Name the parasite shown.
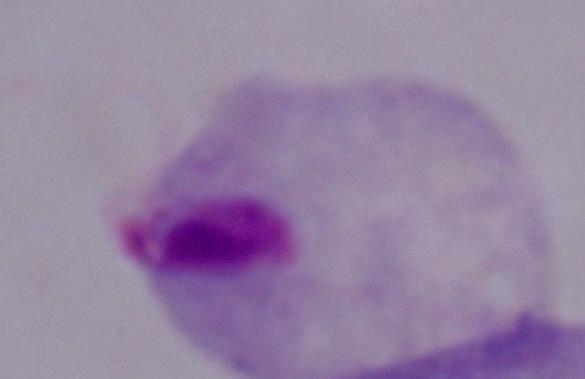
This is a trichomonad.

modality = photomicrograph
magnification = 1000x